Locate and identify every blood parasite.
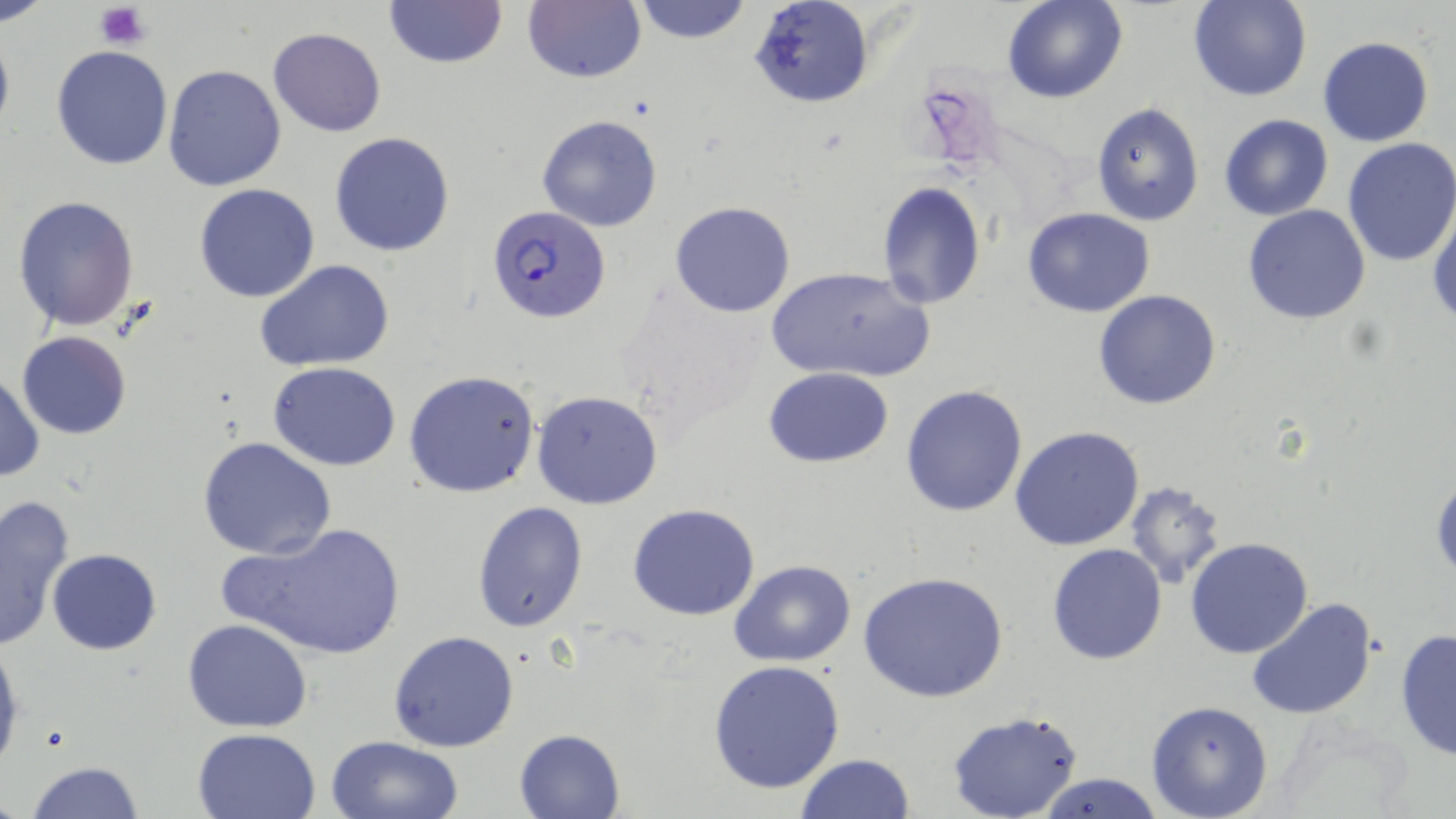
Approximate bounding boxes as [x1, y1, x2, y2] in pixels.
Plasmodium falciparum-infected red blood cells: [489, 204, 611, 323].
No Plasmodium ovale, Plasmodium malariae, Plasmodium vivax, Babesia divergens, or Trypanosoma brucei observed.

{
  "slide_level_diagnosis": "Plasmodium falciparum",
  "platelet_locations": "approximate bounding boxes as [x1, y1, x2, y2] in pixels: [94, 2, 150, 48]",
  "stain": "May-Grünwald-Giemsa",
  "magnification": "1000x",
  "uninfected_red_blood_cell_locations": "approximate bounding boxes as [x1, y1, x2, y2] in pixels: [383, 0, 508, 70], [524, 0, 645, 85], [631, 0, 753, 44], [749, 0, 873, 110], [1003, 0, 1127, 104], [1188, 0, 1311, 102], [0, 25, 15, 141], [268, 27, 388, 136], [1318, 35, 1434, 146], [51, 44, 174, 170], [163, 64, 286, 190], [1091, 101, 1205, 228], [1218, 114, 1334, 221], [537, 115, 662, 232], [330, 132, 455, 257], [1341, 138, 1456, 267], [876, 181, 987, 309], [194, 182, 321, 303], [11, 195, 140, 331], [670, 201, 795, 317], [1242, 205, 1371, 325], [1022, 207, 1154, 316], [1428, 207, 1456, 333], [254, 258, 395, 372], [769, 268, 932, 384], [1094, 289, 1222, 410], [17, 331, 131, 440], [269, 361, 402, 470], [763, 367, 894, 468], [0, 370, 44, 484], [405, 370, 542, 499], [901, 384, 1031, 517], [531, 389, 663, 509], [1010, 425, 1145, 551], [197, 435, 336, 560], [1429, 471, 1455, 582], [1124, 480, 1228, 590], [0, 493, 75, 651], [472, 500, 590, 632], [627, 502, 761, 620], [216, 521, 409, 662], [1185, 537, 1314, 659], [1046, 543, 1167, 665], [47, 548, 162, 656], [730, 560, 856, 668], [859, 570, 1009, 704], [1246, 595, 1379, 720], [182, 620, 314, 733], [1394, 630, 1455, 760], [389, 631, 519, 753], [0, 637, 24, 776], [708, 658, 845, 794], [1145, 700, 1274, 819], [945, 711, 1085, 819], [191, 728, 323, 817], [514, 728, 624, 817], [324, 734, 463, 819], [795, 753, 915, 819], [24, 760, 145, 819], [1037, 772, 1168, 818]",
  "field_of_view": "one of a larger specimen",
  "modality": "light microscopy",
  "image_size": "1456×819 pixels",
  "preparation": "thin blood smear"
}